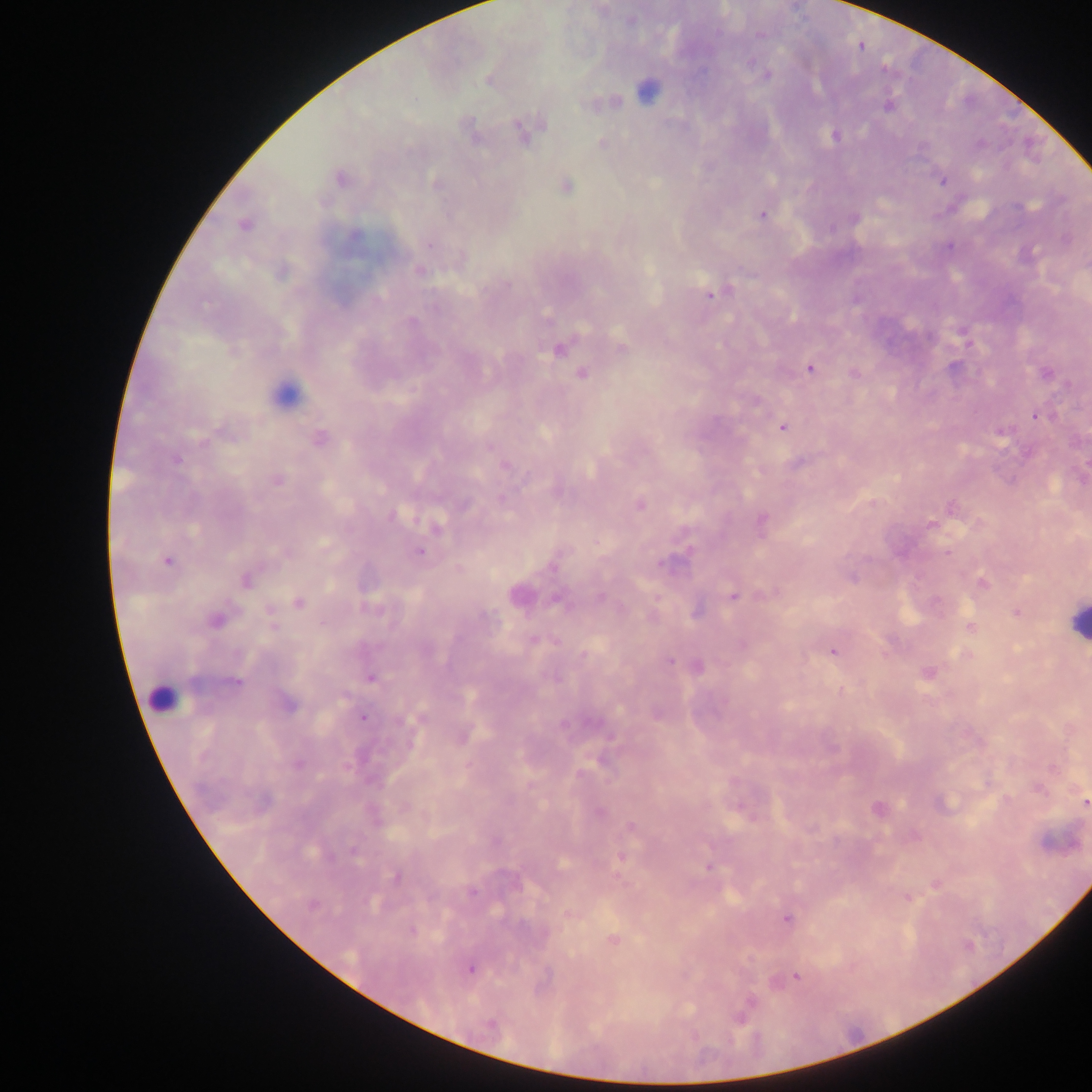

{
  "leukocyte_locations": "approximate centers as (x, y) in pixels: (283, 389), (1077, 622), (162, 699)",
  "country": "Ghana",
  "image_size": "1092×1092 pixels",
  "plasmodium_parasite_locations": "approximate centers as (x, y) in pixels: (631, 19), (767, 74), (647, 89), (603, 103), (887, 106), (470, 132), (523, 132), (835, 136), (603, 143), (340, 178), (942, 179), (435, 183), (566, 185), (762, 214), (854, 217), (245, 224), (950, 245), (1025, 254), (418, 269), (281, 272), (713, 292), (967, 343), (622, 347), (558, 348), (810, 367), (582, 372), (1046, 372), (855, 373), (754, 401), (1036, 415), (782, 426), (1001, 430), (318, 437), (176, 459), (504, 465), (277, 479), (502, 500), (638, 504), (951, 507), (391, 515), (932, 523), (761, 524), (436, 526), (418, 550), (167, 561), (245, 579), (982, 583), (516, 594), (734, 596), (558, 598), (298, 602), (695, 610), (1016, 612), (215, 619), (970, 627), (534, 639), (833, 651), (966, 655), (670, 659), (696, 665), (926, 672), (371, 677), (235, 682), (287, 704), (657, 713), (362, 716), (461, 735), (297, 763), (1085, 803), (877, 809), (631, 827), (622, 856), (707, 866), (396, 876), (935, 884), (906, 896), (569, 914), (787, 918), (411, 930), (612, 938), (469, 968), (797, 976), (750, 1001)",
  "capture": "mobile-phone photograph through a microscope",
  "preparation": "thick blood smear",
  "field_of_view": "single"
}